State which cell type is depicted.
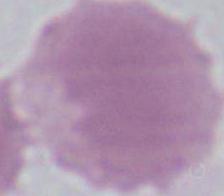

An erythrocyte.

{
  "magnification": "1000x",
  "modality": "photomicrograph"
}